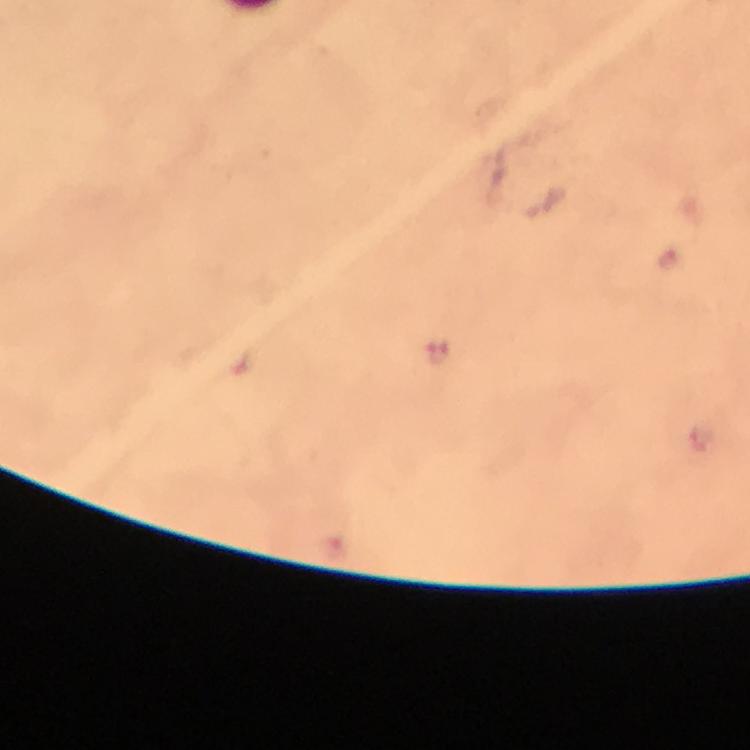
Approximate centers as [x, y] in pixels. Plasmodium parasite locations: [668, 260], [439, 352]. Photographed through the microscope with a smartphone camera. From a malaria diagnostic workup. Immersion oil applied. Thick smear. A crop from one field of view. Image is 750×750 pixels. At 100x magnification. Giemsa stain.